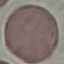

malaria status = uninfected
capture = smartphone camera at the microscope eyepiece
stain = Giemsa
image type = cell patch, automatically extracted from a larger field of view and resized to 64 × 64 pixels
preparation = thin smear